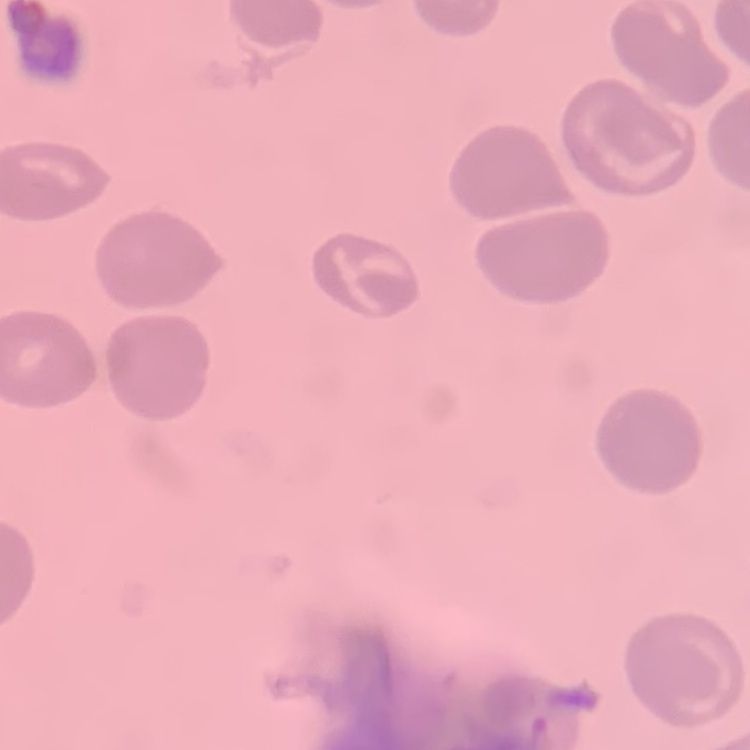 The red blood cells show no rouleaux formation. Field's or Giemsa stain. Thin peripheral smear. One tile cut from a larger photomicrograph.